Locate every uninfected red blood cell.
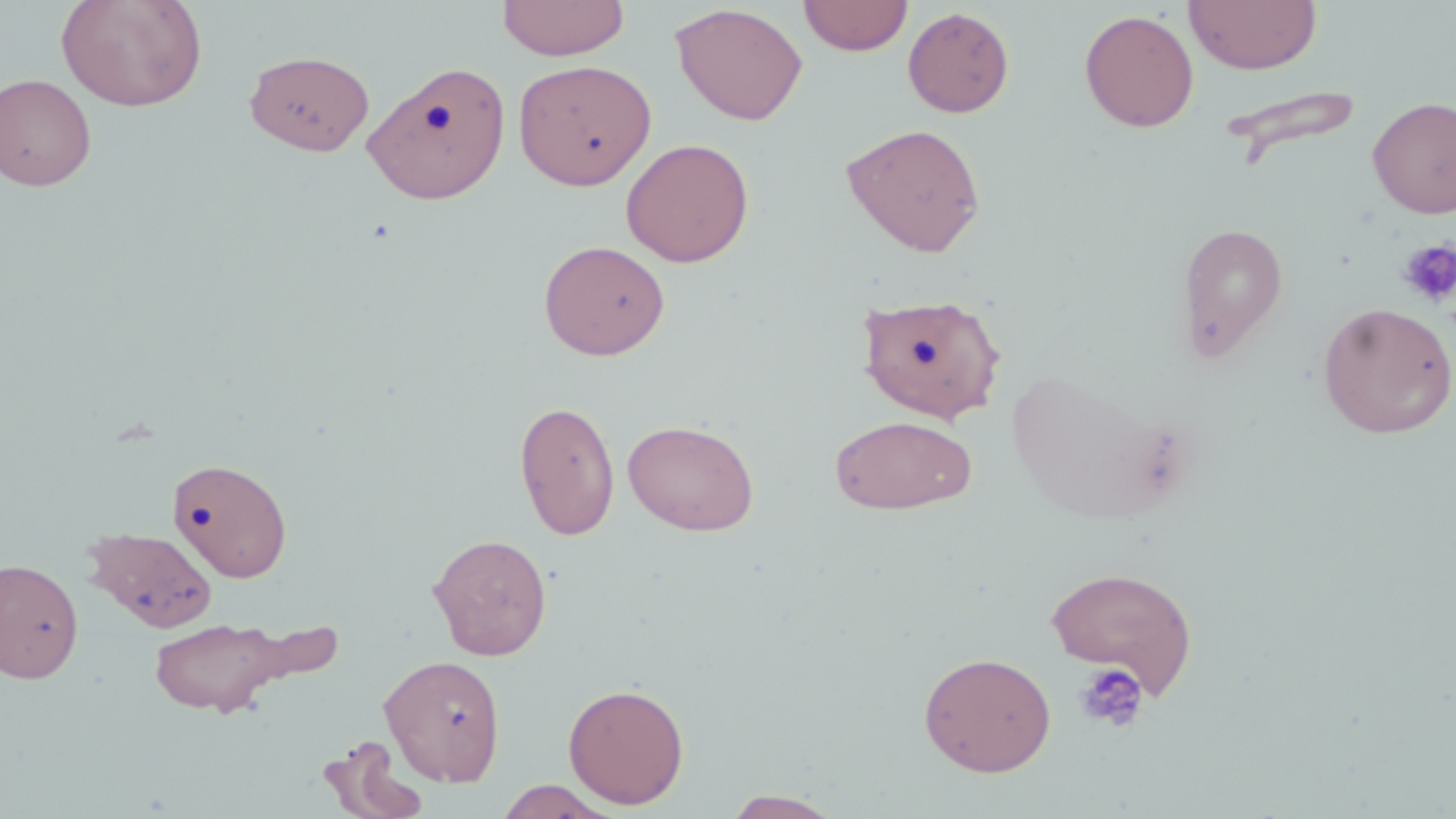

Approximate bounding boxes as named x1/y1/x2/y2 corners in pixels.
Uninfected red blood cells: (x1=56, y1=0, x2=207, y2=112), (x1=497, y1=0, x2=629, y2=60), (x1=797, y1=0, x2=913, y2=56), (x1=1184, y1=0, x2=1321, y2=75), (x1=670, y1=3, x2=808, y2=125), (x1=903, y1=7, x2=1015, y2=117), (x1=1079, y1=9, x2=1199, y2=132), (x1=244, y1=50, x2=374, y2=156), (x1=514, y1=59, x2=657, y2=191), (x1=362, y1=61, x2=511, y2=205), (x1=0, y1=74, x2=97, y2=191), (x1=1213, y1=83, x2=1369, y2=164), (x1=1367, y1=96, x2=1456, y2=218), (x1=840, y1=121, x2=986, y2=257), (x1=620, y1=138, x2=754, y2=267), (x1=1177, y1=222, x2=1290, y2=361), (x1=538, y1=239, x2=670, y2=360), (x1=857, y1=293, x2=1007, y2=423), (x1=1317, y1=301, x2=1456, y2=439), (x1=1005, y1=366, x2=1190, y2=526), (x1=514, y1=399, x2=620, y2=540), (x1=828, y1=414, x2=977, y2=515), (x1=622, y1=419, x2=759, y2=536), (x1=168, y1=456, x2=292, y2=581), (x1=85, y1=526, x2=217, y2=632), (x1=427, y1=532, x2=552, y2=660), (x1=0, y1=557, x2=84, y2=684), (x1=1044, y1=565, x2=1198, y2=696), (x1=148, y1=616, x2=294, y2=718), (x1=918, y1=650, x2=1057, y2=776), (x1=379, y1=654, x2=506, y2=787), (x1=563, y1=682, x2=690, y2=809), (x1=316, y1=735, x2=431, y2=819), (x1=495, y1=779, x2=620, y2=818), (x1=721, y1=789, x2=846, y2=818).

slide_level_diagnosis: negative for blood parasites
image_size: 1456×819 pixels
stain: May-Grünwald-Giemsa
modality: light microscopy
field_of_view: single
magnification: 1000x
platelet_locations: 'approximate bounding boxes as named x1/y1/x2/y2 corners in pixels: (x1=1398, y1=240, x2=1456, y2=307), (x1=1073, y1=662, x2=1150, y2=735)'
preparation: thin blood smear